Assess for parasitized red blood cells.
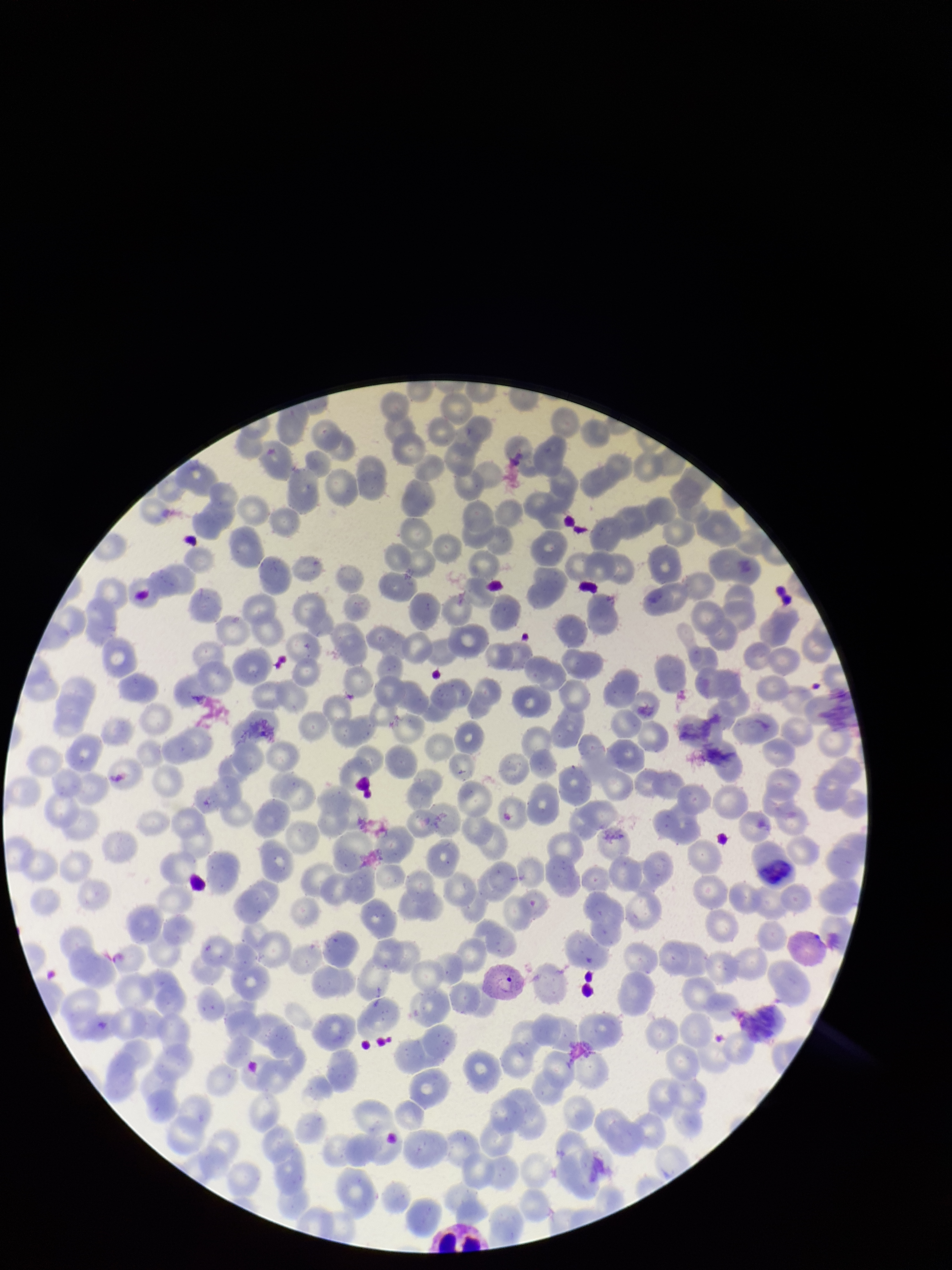
Seen.

{
  "stain": "Giemsa",
  "image_size": "952×1270 pixels",
  "capture": "smartphone photograph through the microscope eyepiece",
  "preparation": "thin",
  "patient_malaria_status": "infected",
  "parasitized_red_blood_cell_count": 2,
  "field_of_view": "single",
  "red_blood_cell_count": 217,
  "species_reported_for_this_patient": "Plasmodium vivax"
}